Outline each blood parasite and name the species.
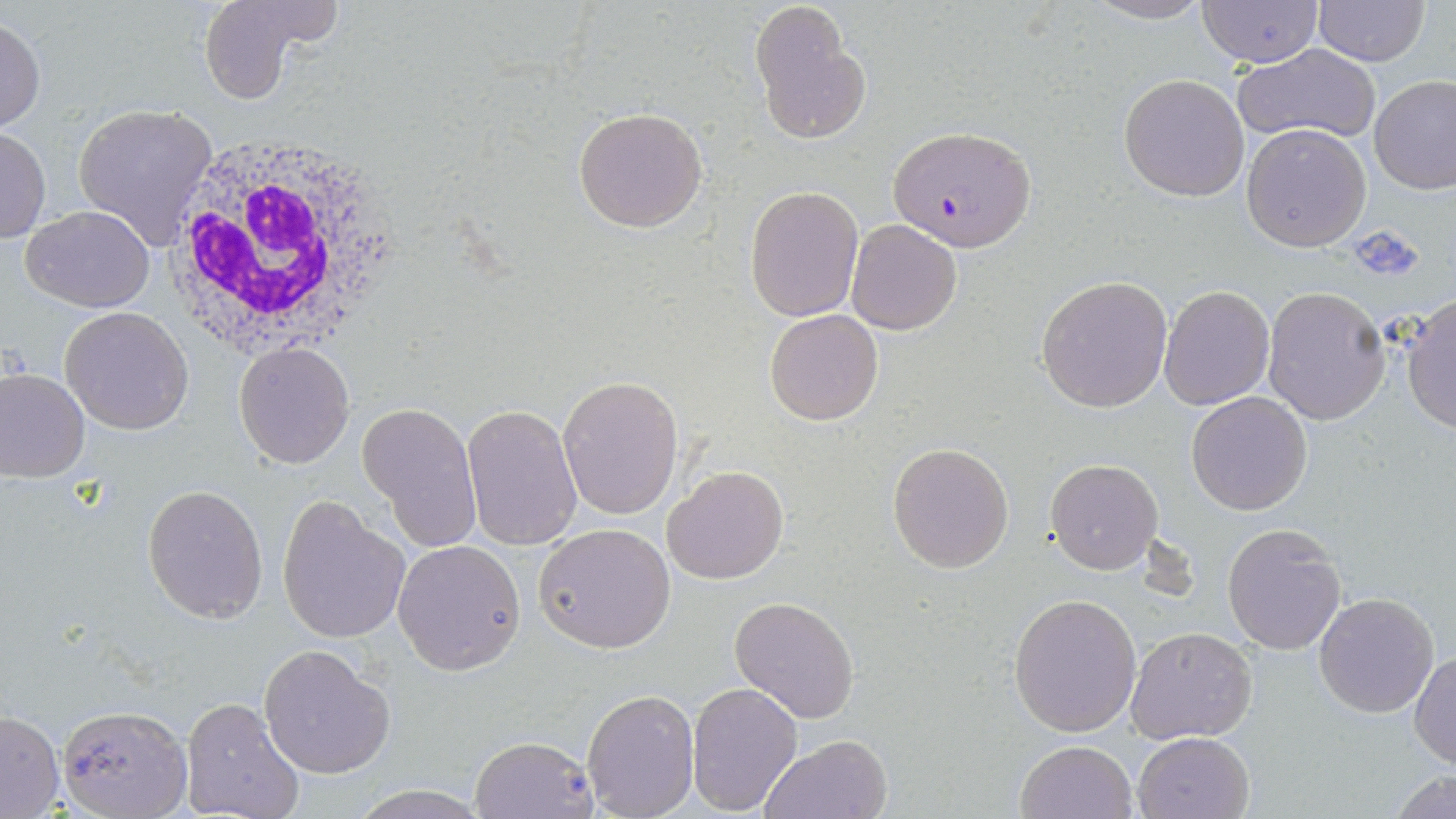

Approximate bounding boxes as (x1, y1, x2, y2) in pixels.
Plasmodium falciparum-infected red blood cells: (888, 125, 1037, 252).
No Plasmodium ovale, Plasmodium malariae, Plasmodium vivax, Babesia divergens, or Trypanosoma brucei observed.

slide-level diagnosis = Plasmodium falciparum
white blood cell locations = approximate bounding boxes as (x1, y1, x2, y2) in pixels: (162, 135, 403, 356)
uninfected red blood cell locations = approximate bounding boxes as (x1, y1, x2, y2) in pixels: (195, 0, 340, 105), (1086, 1, 1214, 24), (1312, 1, 1430, 65), (1198, 2, 1326, 67), (748, 4, 866, 144), (0, 14, 46, 133), (1233, 42, 1382, 145), (1369, 73, 1456, 194), (1119, 74, 1250, 202), (72, 102, 220, 245), (572, 106, 710, 232), (1241, 122, 1372, 252), (1, 124, 49, 245), (746, 185, 863, 323), (22, 206, 155, 311), (846, 220, 962, 335), (1036, 274, 1173, 412), (1158, 284, 1275, 409), (1262, 287, 1391, 424), (1402, 294, 1456, 434), (58, 306, 193, 434), (764, 308, 883, 425), (234, 342, 355, 468), (0, 366, 91, 482), (557, 374, 683, 521), (1186, 392, 1312, 515), (358, 401, 482, 551), (461, 402, 582, 551), (887, 441, 1015, 575), (1046, 458, 1161, 573), (662, 464, 789, 585), (143, 484, 268, 623), (277, 496, 409, 645), (1222, 522, 1347, 653), (533, 523, 676, 653), (393, 539, 526, 674), (1313, 591, 1440, 717), (1009, 593, 1142, 736), (729, 595, 860, 724), (1124, 626, 1259, 745), (258, 643, 394, 777), (1410, 651, 1455, 768), (686, 681, 804, 815), (581, 689, 700, 818), (180, 696, 306, 819), (57, 704, 192, 819), (0, 709, 65, 817), (1132, 731, 1256, 819), (468, 735, 600, 818), (759, 736, 892, 819), (1015, 740, 1139, 819), (1385, 770, 1456, 819), (344, 786, 494, 818)
stain = May-Grünwald-Giemsa
magnification = 1000x
preparation = thin blood film
image size = 1456×819 pixels
modality = light microscopy
platelet locations = approximate bounding boxes as (x1, y1, x2, y2) in pixels: (1347, 224, 1428, 285)
field of view = single